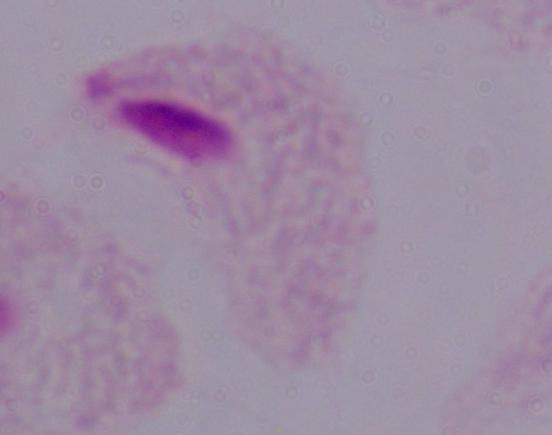

identification = trichomonad
modality = photomicrograph
magnification = 1000x